Report the malaria status of this cell.
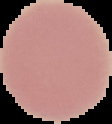
Uninfected.

Image is 112×124 pixels. From a thin blood smear. Segmented cell region on a black background.